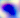
identification = Toxoplasma gondii
modality = photomicrograph
magnification = 400x